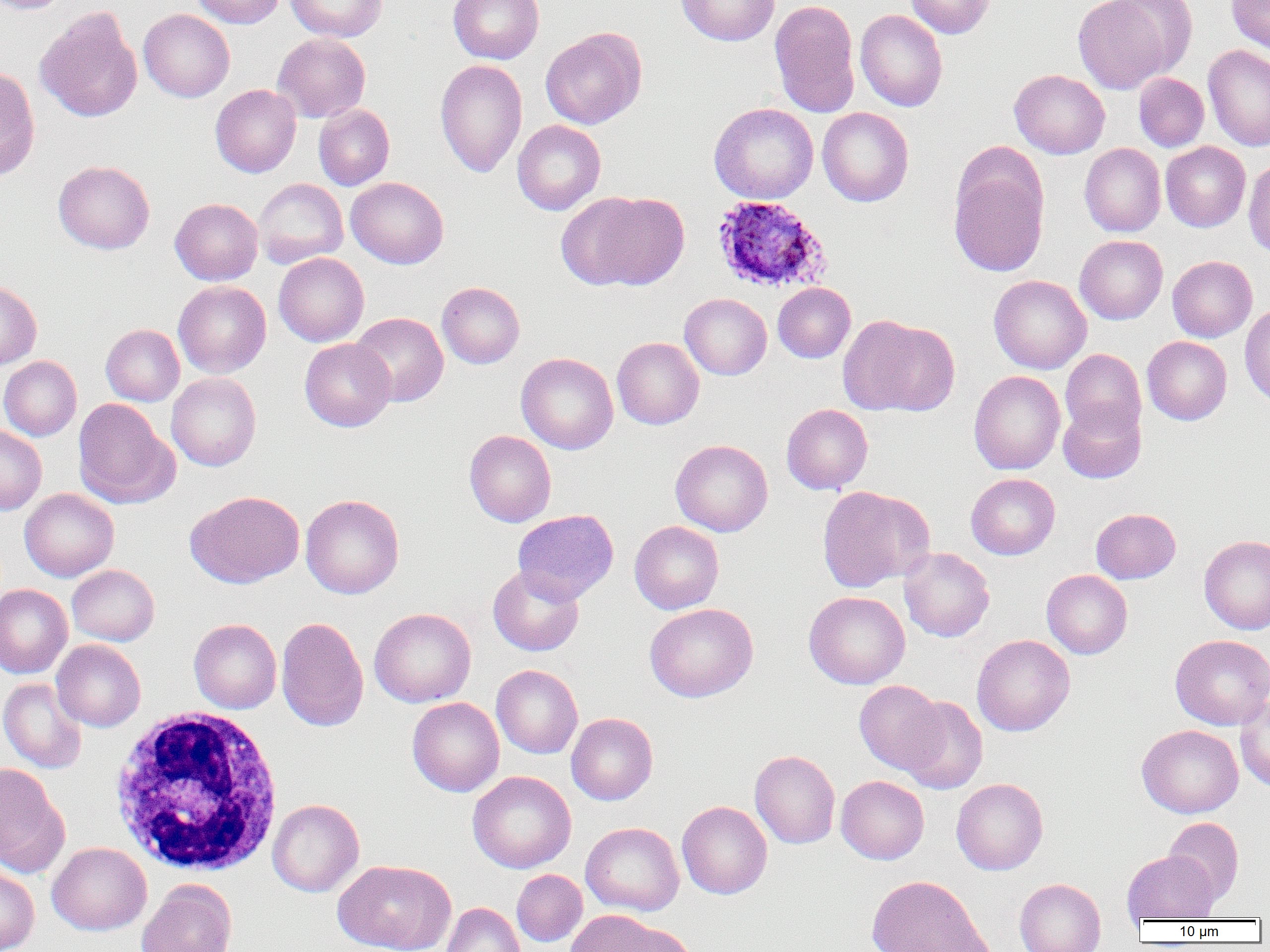

Approximate bounding boxes as [x1, y1, x2, y2] in pixels. White blood cell locations: [109, 707, 286, 877]. Uninfected red blood cell locations: [0, 0, 72, 14], [190, 0, 286, 28], [285, 0, 388, 42], [448, 0, 544, 64], [676, 0, 780, 46], [769, 0, 861, 118], [905, 0, 995, 39], [1072, 0, 1177, 94], [1226, 0, 1270, 55], [35, 7, 142, 123], [138, 9, 235, 102], [855, 9, 948, 112], [540, 27, 647, 129], [272, 33, 371, 122], [1203, 44, 1270, 151], [435, 59, 527, 178], [0, 66, 41, 182], [1009, 69, 1110, 159], [1133, 72, 1210, 151], [210, 84, 301, 178], [709, 102, 819, 204], [313, 104, 394, 190], [817, 107, 914, 207], [512, 120, 606, 215], [1161, 142, 1251, 232], [1079, 143, 1166, 237], [948, 155, 1049, 278], [1243, 157, 1270, 258], [53, 160, 155, 254], [346, 177, 448, 268], [254, 178, 348, 268], [561, 191, 689, 291], [170, 198, 263, 285], [1074, 235, 1168, 324], [273, 252, 369, 346], [1167, 255, 1257, 342], [988, 275, 1092, 374], [0, 280, 41, 370], [173, 281, 271, 378], [437, 282, 525, 369], [773, 283, 855, 363], [679, 293, 772, 380], [1239, 301, 1270, 407], [350, 312, 449, 407], [839, 315, 960, 417], [101, 324, 184, 406], [1142, 336, 1232, 425], [612, 337, 704, 429], [299, 338, 396, 432], [1060, 349, 1146, 440], [516, 352, 618, 454], [0, 356, 82, 440], [969, 370, 1065, 474], [166, 372, 261, 471], [73, 398, 177, 509], [1058, 401, 1146, 484], [781, 404, 873, 494], [0, 426, 47, 515], [464, 430, 556, 527], [670, 439, 773, 537], [966, 473, 1060, 559], [818, 485, 933, 592], [20, 488, 119, 582], [185, 490, 305, 588], [301, 494, 404, 599], [1091, 508, 1181, 583], [512, 509, 618, 603], [629, 520, 724, 614], [1199, 535, 1270, 634], [898, 547, 994, 642], [67, 565, 160, 646], [488, 565, 584, 656], [1041, 570, 1133, 659], [0, 584, 72, 679], [804, 590, 910, 689], [644, 603, 758, 702], [369, 607, 476, 708], [276, 617, 369, 731], [189, 618, 282, 714], [971, 634, 1075, 736], [1170, 634, 1270, 730], [52, 640, 146, 732], [492, 665, 583, 758], [0, 677, 87, 774], [854, 680, 946, 774], [896, 696, 988, 794], [1235, 696, 1270, 792], [407, 697, 504, 797], [566, 713, 658, 805], [1137, 724, 1243, 818], [750, 750, 840, 849], [0, 764, 68, 876], [467, 771, 576, 873], [835, 775, 930, 864], [951, 778, 1048, 875], [267, 798, 365, 897], [677, 801, 772, 899], [1163, 817, 1244, 906], [581, 822, 684, 916], [47, 842, 152, 935], [1122, 850, 1218, 922], [332, 859, 455, 952], [0, 864, 39, 952], [512, 869, 587, 947], [867, 874, 991, 951], [1014, 878, 1106, 952], [137, 880, 238, 952], [441, 902, 526, 952], [564, 910, 671, 951], [608, 922, 698, 952]. Plasmodium ovale-infected red blood cell locations: [711, 195, 832, 295]. Slide-level diagnosis: Plasmodium ovale. Light microscopy. Captured at 1000x magnification. Image is 1270×952 pixels. Thin blood smear. Single field of view.